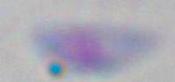
modality: micrograph
identification: Toxoplasma gondii
magnification: 1000x